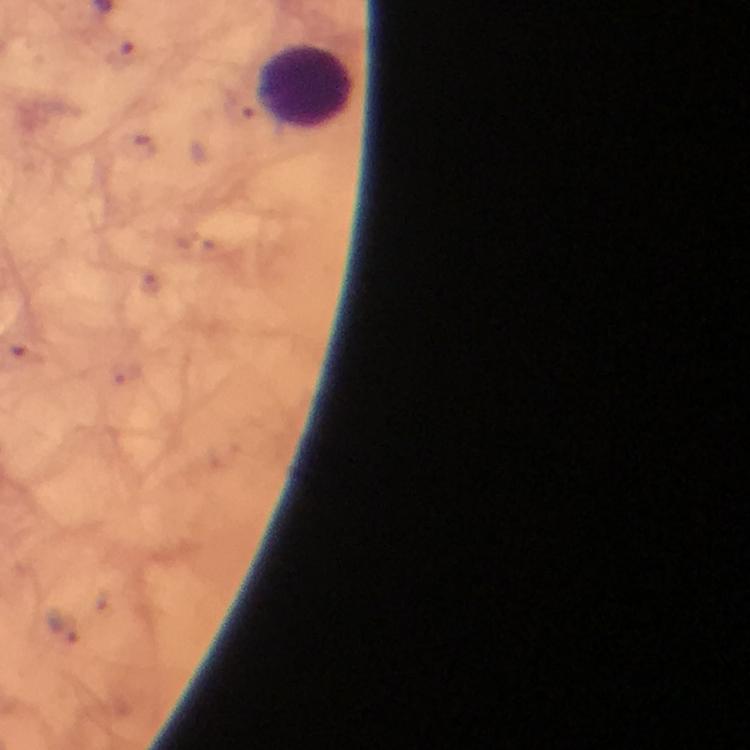

preparation = thick smear
capture = smartphone camera through the microscope
context = from a diagnostic examination for malaria
image size = 750×750 pixels
leukocyte locations = approximate object centers, in pixels from the top-left corner: (x=306, y=89)
stain = Giemsa
cropped from = a single field of view
immersion oil = used
malaria parasites = none seen
magnification = 100x